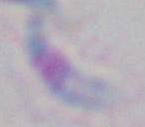
Photomicrograph. Captured at 1000x magnification. Toxoplasma gondii is shown.